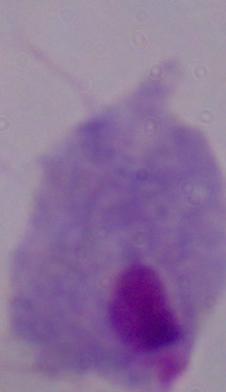
A trichomonad is seen. Captured at 1000x magnification. Photomicrograph.